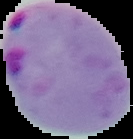
Summary:
  - Image type: segmented cell region with the area outside set to black
  - Image size: 133×139 pixels
  - Result: malaria parasites identified
  - Preparation: thin blood film